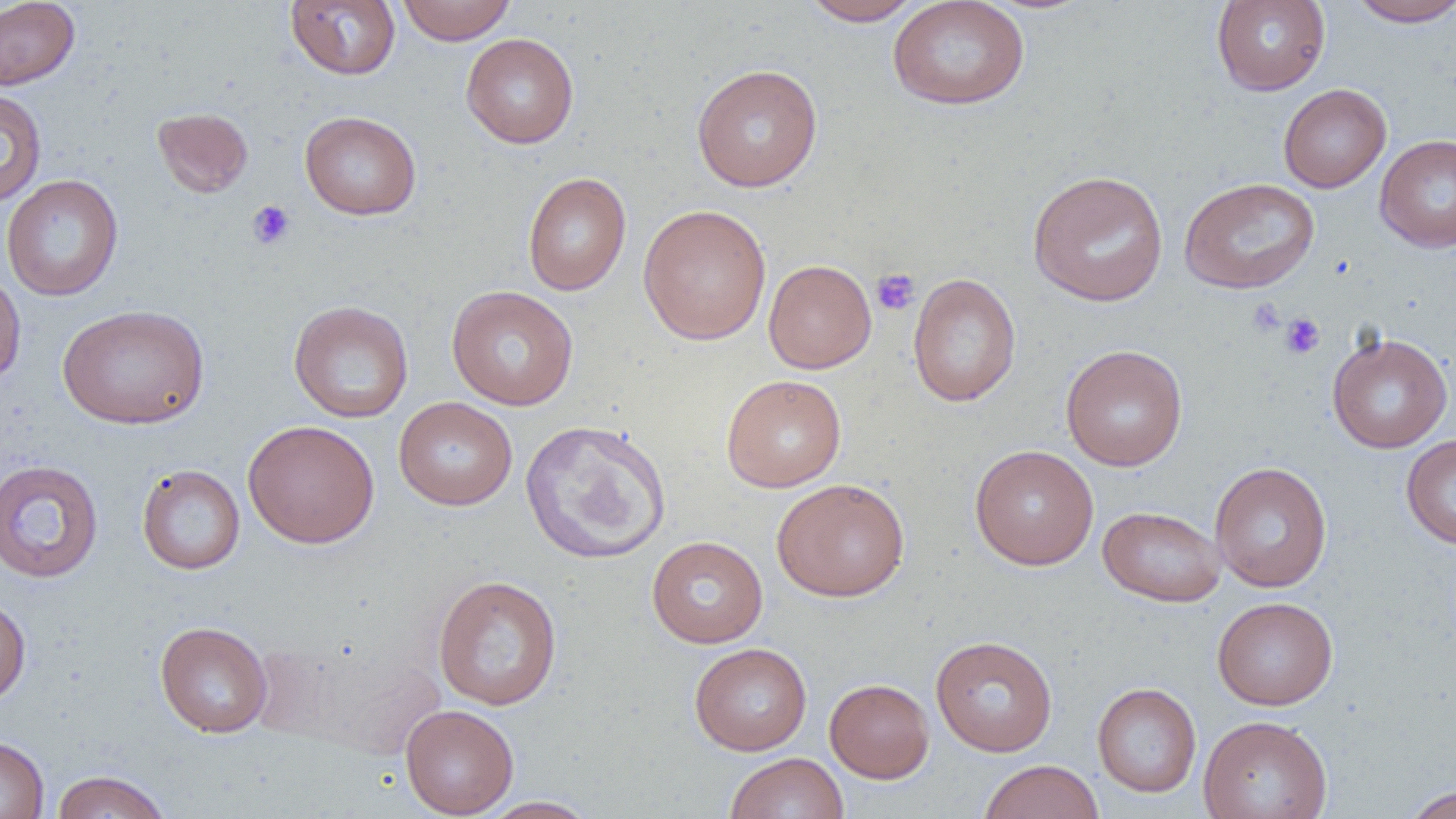
Summary:
  - Coordinate format: approximate bounding boxes as named x1/y1/x2/y2 corners in pixels
  - Uninfected red blood cell locations: (x1=0, y1=0, x2=81, y2=90), (x1=285, y1=0, x2=401, y2=79), (x1=397, y1=0, x2=515, y2=45), (x1=799, y1=0, x2=926, y2=26), (x1=887, y1=0, x2=1030, y2=110), (x1=1211, y1=0, x2=1330, y2=96), (x1=1346, y1=0, x2=1456, y2=27), (x1=460, y1=32, x2=579, y2=149), (x1=690, y1=63, x2=823, y2=192), (x1=1278, y1=84, x2=1392, y2=193), (x1=0, y1=88, x2=48, y2=207), (x1=152, y1=106, x2=253, y2=198), (x1=299, y1=111, x2=421, y2=220), (x1=1375, y1=134, x2=1456, y2=253), (x1=1027, y1=169, x2=1168, y2=306), (x1=522, y1=172, x2=631, y2=296), (x1=1, y1=174, x2=124, y2=302), (x1=1179, y1=177, x2=1319, y2=294), (x1=637, y1=204, x2=772, y2=345), (x1=763, y1=259, x2=877, y2=374), (x1=0, y1=268, x2=26, y2=389), (x1=907, y1=273, x2=1022, y2=407), (x1=446, y1=285, x2=579, y2=411), (x1=288, y1=300, x2=414, y2=423), (x1=57, y1=304, x2=211, y2=429), (x1=1326, y1=332, x2=1453, y2=453), (x1=1060, y1=344, x2=1188, y2=471), (x1=721, y1=374, x2=846, y2=492), (x1=393, y1=396, x2=518, y2=511), (x1=243, y1=419, x2=380, y2=548), (x1=520, y1=419, x2=671, y2=564), (x1=1401, y1=434, x2=1456, y2=550), (x1=969, y1=444, x2=1099, y2=570), (x1=0, y1=459, x2=104, y2=584), (x1=1209, y1=461, x2=1332, y2=592), (x1=136, y1=464, x2=245, y2=574), (x1=772, y1=477, x2=910, y2=601), (x1=1098, y1=505, x2=1227, y2=607), (x1=646, y1=535, x2=768, y2=648), (x1=432, y1=574, x2=563, y2=711), (x1=0, y1=594, x2=31, y2=707), (x1=1212, y1=596, x2=1338, y2=710), (x1=155, y1=621, x2=273, y2=737), (x1=930, y1=635, x2=1058, y2=757), (x1=296, y1=642, x2=448, y2=759), (x1=689, y1=642, x2=812, y2=755), (x1=824, y1=678, x2=935, y2=783), (x1=1092, y1=682, x2=1202, y2=798), (x1=400, y1=704, x2=519, y2=817), (x1=1198, y1=714, x2=1333, y2=819), (x1=0, y1=734, x2=49, y2=819), (x1=724, y1=752, x2=849, y2=819), (x1=978, y1=759, x2=1104, y2=819), (x1=50, y1=769, x2=172, y2=819), (x1=1401, y1=785, x2=1456, y2=819), (x1=477, y1=796, x2=600, y2=818)
  - Platelet locations: (x1=247, y1=200, x2=296, y2=250), (x1=872, y1=268, x2=920, y2=316), (x1=1247, y1=298, x2=1285, y2=336), (x1=1280, y1=313, x2=1325, y2=360)
  - Slide-level diagnosis: negative for blood parasites
  - Field of view: single
  - Image size: 1456×819 pixels
  - Modality: light microscopy
  - Preparation: thin blood film
  - Magnification: 1000x